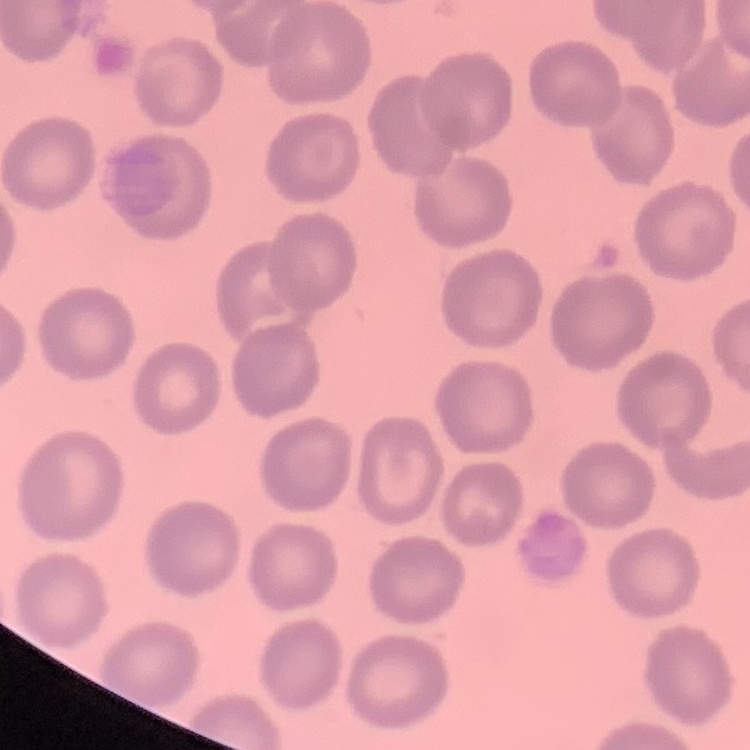
erythrocyte morphology = no rouleaux formation
preparation = thin blood smear
image type = square crop of a larger photomicrograph
stain = Field's or Giemsa